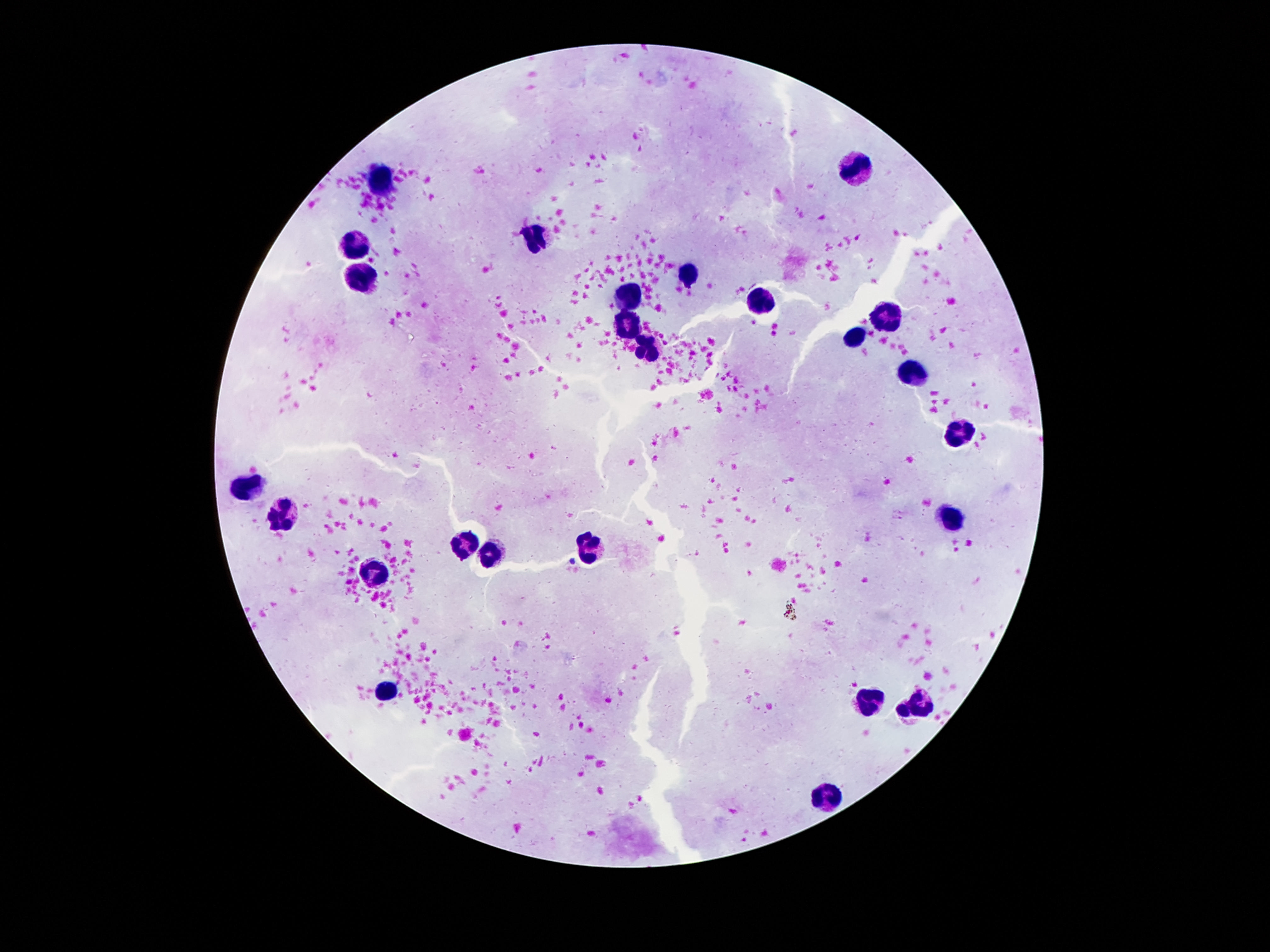
Approximate object centers, in pixels from the top-left corner.
Summary:
  - Leukocyte locations: (x=858, y=168), (x=384, y=178), (x=538, y=234), (x=359, y=240), (x=365, y=273), (x=690, y=276), (x=631, y=297), (x=760, y=300), (x=888, y=318), (x=629, y=324), (x=855, y=338), (x=648, y=350), (x=911, y=367), (x=956, y=434), (x=253, y=488), (x=288, y=514), (x=949, y=519), (x=468, y=549), (x=590, y=549), (x=491, y=560), (x=373, y=572), (x=389, y=691), (x=870, y=703), (x=912, y=709), (x=827, y=795)
  - Field of view: one from this slide
  - Magnification: 100x
  - Stain: Giemsa
  - Image size: 1270×952 pixels
  - Preparation: thick blood smear
  - Patient malaria status: negative
  - Capture: smartphone camera through the microscope eyepiece